Name the parasite shown.
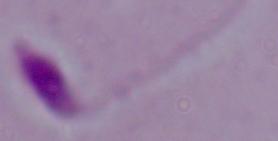
Leishmania.

magnification = 1000x
modality = micrograph